Assess this cell for malaria.
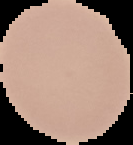

Uninfected.

Image is 133×145 pixels. From a thin blood film. Cell region segmented out of the field of view; the surrounding area is masked to black.